Comment on the morphology of the red blood cells.
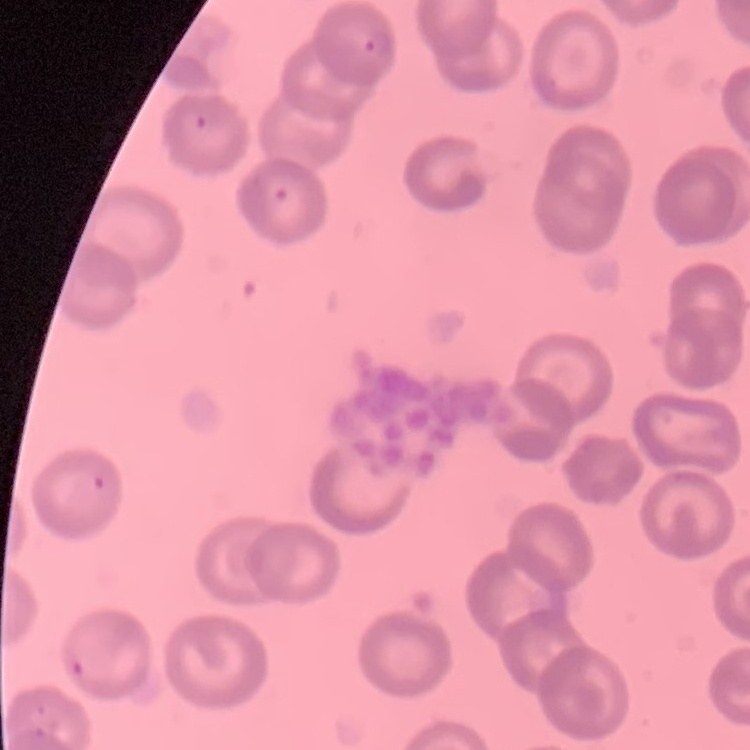
No rouleaux formation.

Stained with either Field's or Giemsa. Square crop of a larger photomicrograph. Thin blood film.